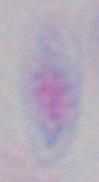

modality = photomicrograph
magnification = 1000x
identification = Toxoplasma gondii